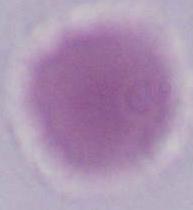 Micrograph. A red blood cell is seen. 1000x magnification.